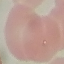

{
  "malaria_status": "parasitized",
  "image_type": "automatically extracted cell patch, resized to 64 × 64 pixels",
  "capture": "smartphone through the microscope eyepiece",
  "stain": "Giemsa",
  "preparation": "thin smear"
}